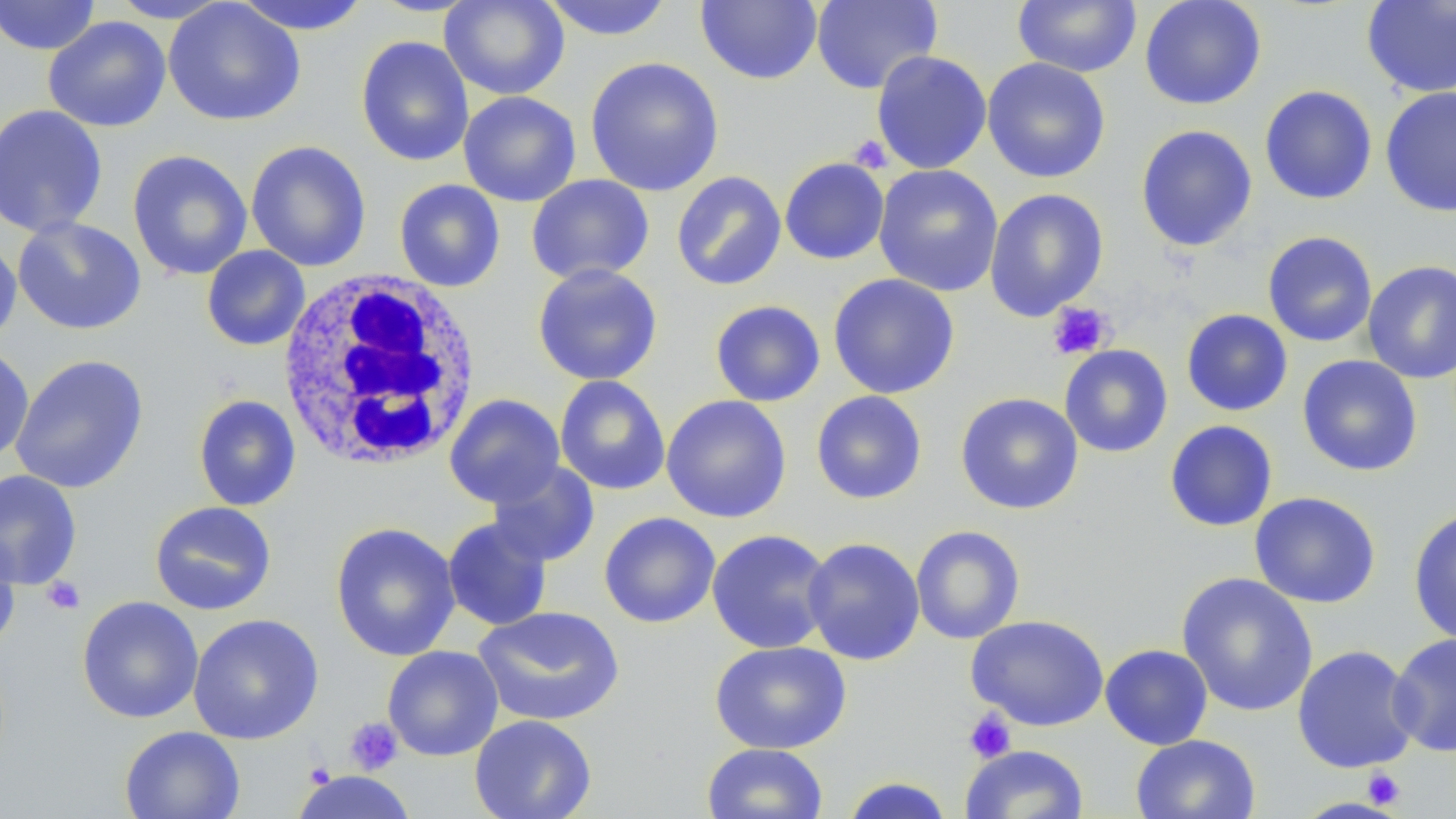
Summary:
  - Coordinate format: approximate bounding boxes as named x1/y1/x2/y2 corners in pixels
  - Uninfected red blood cell locations: (x1=0, y1=0, x2=101, y2=56), (x1=109, y1=0, x2=231, y2=23), (x1=162, y1=0, x2=306, y2=127), (x1=231, y1=0, x2=372, y2=35), (x1=440, y1=0, x2=570, y2=100), (x1=539, y1=0, x2=675, y2=41), (x1=696, y1=0, x2=823, y2=85), (x1=811, y1=0, x2=942, y2=94), (x1=1012, y1=0, x2=1142, y2=77), (x1=1139, y1=0, x2=1267, y2=110), (x1=1361, y1=1, x2=1456, y2=98), (x1=43, y1=16, x2=172, y2=133), (x1=355, y1=36, x2=474, y2=167), (x1=871, y1=50, x2=992, y2=174), (x1=584, y1=56, x2=724, y2=197), (x1=982, y1=57, x2=1111, y2=182), (x1=1259, y1=86, x2=1377, y2=205), (x1=1380, y1=87, x2=1456, y2=217), (x1=458, y1=91, x2=581, y2=207), (x1=0, y1=103, x2=108, y2=239), (x1=1136, y1=124, x2=1258, y2=252), (x1=245, y1=140, x2=372, y2=272), (x1=127, y1=150, x2=253, y2=281), (x1=780, y1=157, x2=890, y2=265), (x1=873, y1=164, x2=1004, y2=297), (x1=671, y1=171, x2=786, y2=291), (x1=526, y1=174, x2=655, y2=286), (x1=394, y1=179, x2=505, y2=292), (x1=984, y1=188, x2=1109, y2=321), (x1=12, y1=216, x2=147, y2=335), (x1=1262, y1=231, x2=1377, y2=348), (x1=0, y1=235, x2=21, y2=350), (x1=201, y1=245, x2=310, y2=351), (x1=1362, y1=259, x2=1456, y2=384), (x1=532, y1=262, x2=664, y2=386), (x1=828, y1=273, x2=960, y2=399), (x1=710, y1=300, x2=825, y2=407), (x1=1181, y1=309, x2=1293, y2=416), (x1=1059, y1=344, x2=1173, y2=458), (x1=1, y1=345, x2=35, y2=464), (x1=10, y1=354, x2=149, y2=494), (x1=1297, y1=355, x2=1423, y2=477), (x1=554, y1=375, x2=670, y2=496), (x1=810, y1=390, x2=928, y2=504), (x1=955, y1=392, x2=1084, y2=515), (x1=444, y1=393, x2=565, y2=508), (x1=193, y1=394, x2=301, y2=512), (x1=661, y1=394, x2=792, y2=524), (x1=1164, y1=420, x2=1278, y2=532), (x1=487, y1=460, x2=600, y2=567), (x1=0, y1=469, x2=82, y2=590), (x1=1249, y1=491, x2=1381, y2=609), (x1=149, y1=501, x2=277, y2=616), (x1=1408, y1=507, x2=1456, y2=646), (x1=599, y1=512, x2=721, y2=629), (x1=442, y1=516, x2=554, y2=631), (x1=330, y1=522, x2=461, y2=661), (x1=910, y1=525, x2=1025, y2=644), (x1=0, y1=527, x2=21, y2=653), (x1=707, y1=529, x2=834, y2=654), (x1=802, y1=537, x2=925, y2=665), (x1=1177, y1=572, x2=1318, y2=717), (x1=77, y1=596, x2=204, y2=723), (x1=472, y1=606, x2=625, y2=727), (x1=188, y1=613, x2=325, y2=745), (x1=966, y1=614, x2=1109, y2=732), (x1=1387, y1=632, x2=1456, y2=757), (x1=710, y1=640, x2=851, y2=754), (x1=1100, y1=643, x2=1213, y2=750), (x1=382, y1=645, x2=503, y2=761), (x1=1292, y1=645, x2=1419, y2=773), (x1=469, y1=714, x2=597, y2=819), (x1=119, y1=726, x2=245, y2=819), (x1=1131, y1=733, x2=1261, y2=819), (x1=701, y1=743, x2=828, y2=819), (x1=960, y1=744, x2=1089, y2=819), (x1=293, y1=770, x2=416, y2=819), (x1=841, y1=776, x2=954, y2=818)
  - Platelet locations: (x1=848, y1=134, x2=893, y2=173), (x1=1047, y1=302, x2=1115, y2=360), (x1=42, y1=576, x2=85, y2=615), (x1=963, y1=709, x2=1017, y2=763), (x1=345, y1=718, x2=402, y2=774), (x1=304, y1=762, x2=336, y2=788), (x1=1361, y1=768, x2=1406, y2=809)
  - White blood cell locations: (x1=275, y1=269, x2=481, y2=472)
  - Slide-level diagnosis: no evidence of blood parasites
  - Modality: light microscopy
  - Field of view: one of a larger specimen
  - Magnification: 1000x
  - Stain: May-Grünwald-Giemsa
  - Image size: 1456×819 pixels
  - Preparation: thin blood smear